Classify this cell by malaria status.
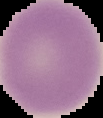
Uninfected.

Summary:
  - Image size: 103×118 pixels
  - Preparation: thin blood smear
  - Image type: segmented cell region with the area outside set to black